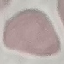
Summary:
  - Malaria status: uninfected
  - Preparation: thin smear
  - Capture: smartphone camera at the microscope eyepiece
  - Stain: Giemsa
  - Image type: cell patch, automatically extracted from a larger field of view and resized to 64 × 64 pixels